Point out each leukocyte.
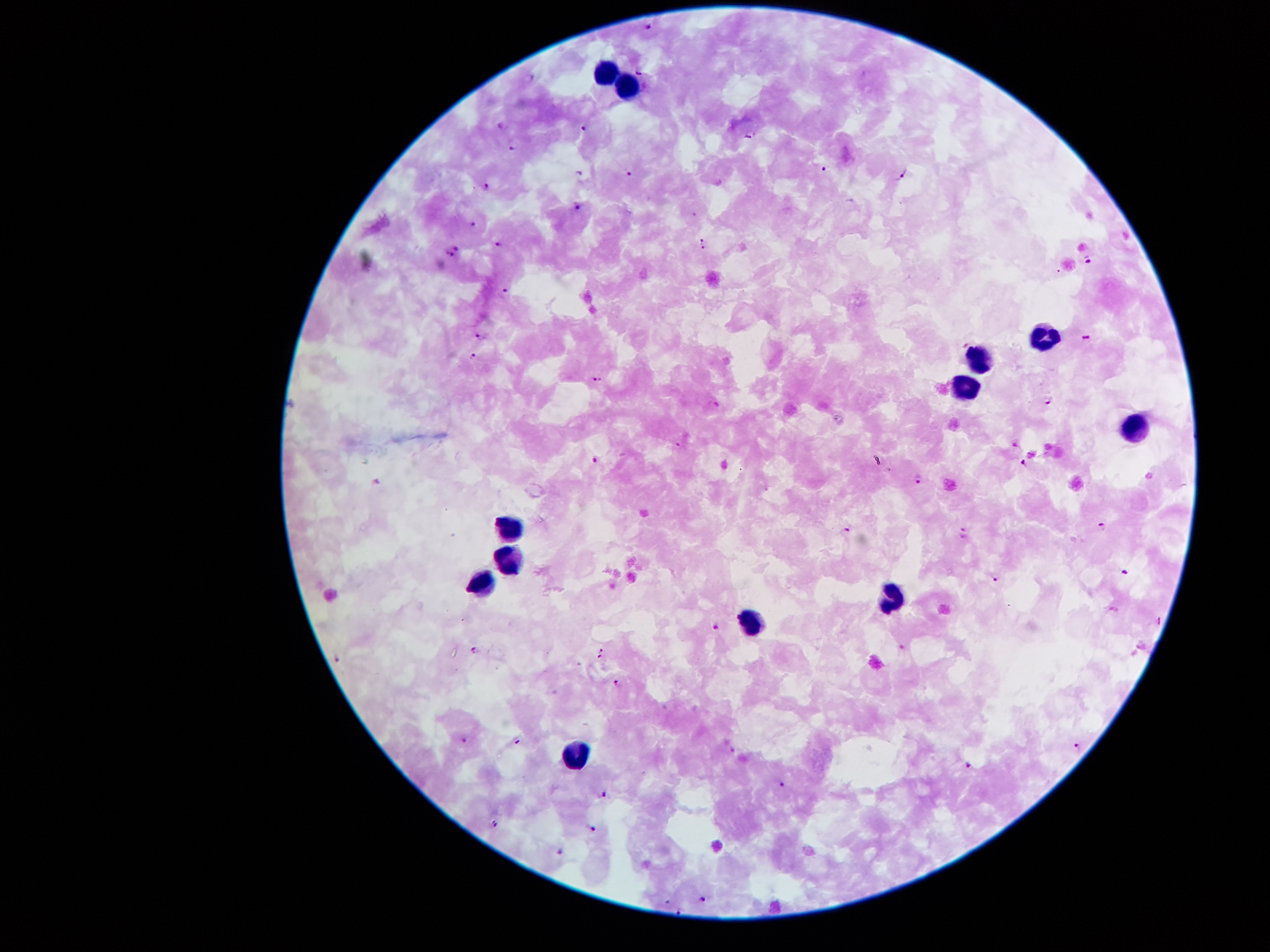

Approximate centers as (x, y) in pixels.
Leukocytes: (607, 70), (628, 82), (1043, 335), (979, 358), (963, 384), (1132, 429), (510, 524), (507, 559), (483, 579), (893, 594), (752, 619), (575, 755).

Malaria parasite locations: (651, 28), (641, 72), (533, 75), (583, 128), (750, 134), (513, 147), (823, 168), (578, 171), (629, 172), (902, 179), (486, 186), (577, 206), (474, 223), (701, 238), (496, 243), (455, 247), (702, 249), (450, 256), (1090, 260), (505, 290), (480, 338), (1084, 339), (474, 355), (597, 379), (1049, 402), (679, 445), (594, 459), (1024, 463), (919, 480), (1103, 526), (964, 531), (846, 532), (1126, 571), (997, 579), (1159, 618), (717, 627), (475, 647), (602, 647), (599, 658), (619, 682), (464, 738), (517, 742), (1078, 747), (969, 766), (783, 784), (605, 795), (495, 823), (594, 828), (561, 853), (703, 898), (681, 910). Giemsa stain. Smartphone photograph taken through the microscope eyepiece. Thick blood film. Patient malaria status: infected with Plasmodium falciparum. 100x magnification. Image is 1270×952 pixels. Single field of view.